Comment on the morphology of the erythrocytes.
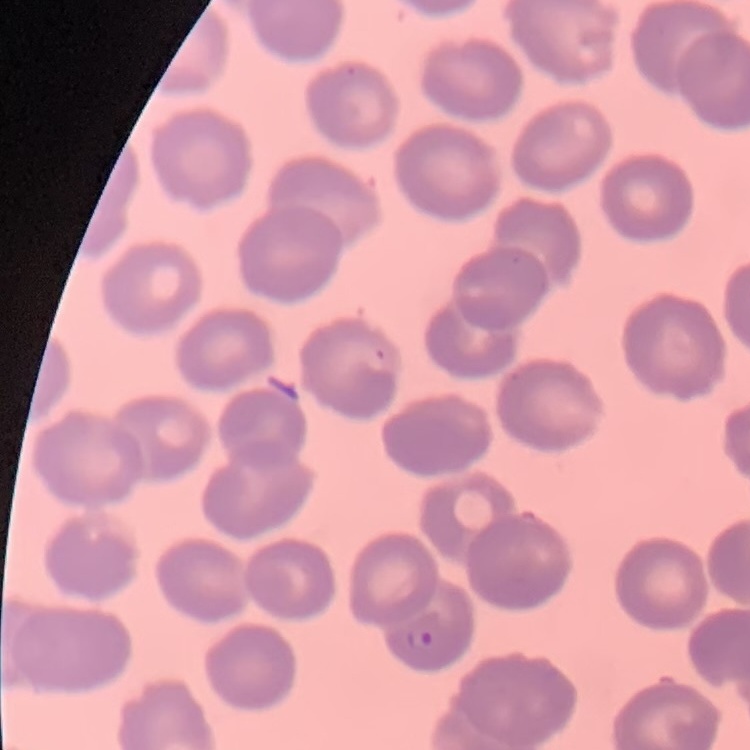
No rouleaux formation.

Square crop of a larger photomicrograph. Field's or Giemsa stain. Thin blood smear.